Report the malaria status of this cell.
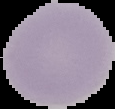

It is uninfected.

{
  "preparation": "thin blood film",
  "image_size": "115×109 pixels",
  "image_type": "segmented cell region on a black background"
}